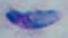
Summary:
  - Identification: Toxoplasma gondii
  - Magnification: 1000x
  - Modality: photomicrograph